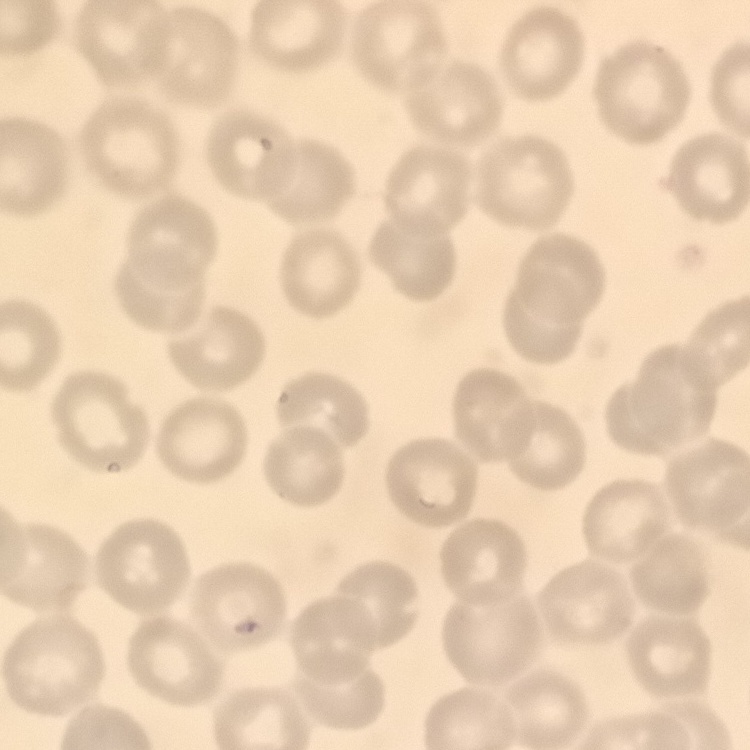

Summary:
  - Red blood cell morphology: no rouleaux formation
  - Image type: one tile cut from a larger photomicrograph
  - Stain: Field's or Giemsa
  - Preparation: thin peripheral smear